Give a bounding box for every leukocyte visible.
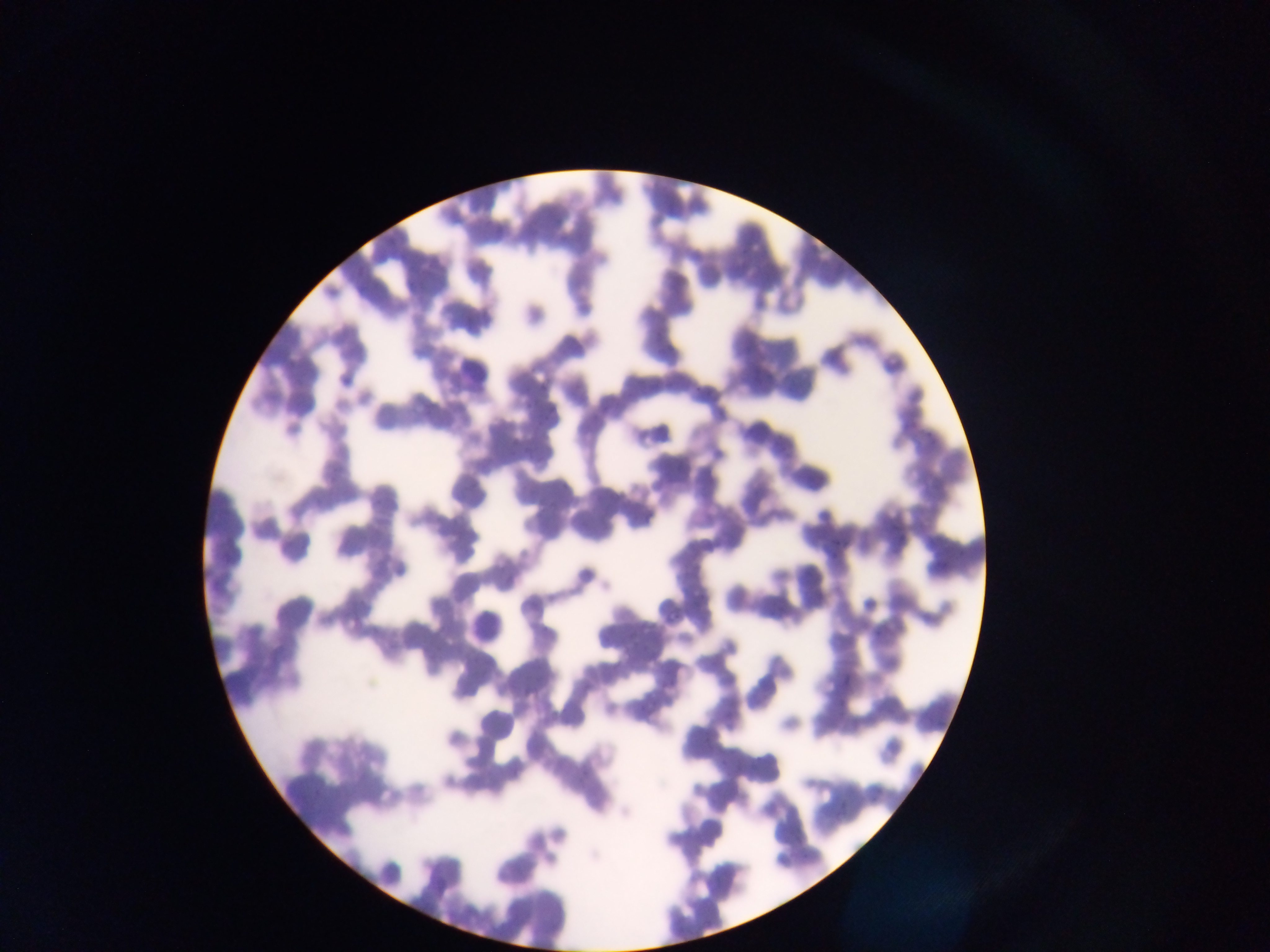
Approximate bounding boxes as (left, top, right, bottom) in pixels.
Leukocytes: (449, 348, 492, 389), (779, 452, 841, 504), (463, 597, 518, 658).

capture = mobile-phone photograph through a microscope
field of view = single
image size = 1270×952 pixels
country = Ghana
preparation = thin blood film